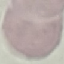
Result: no malaria parasites detected. Acquired by smartphone through the microscope eyepiece. Cell patch, automatically extracted from a larger field of view and resized to 64 × 64 pixels. Thin blood smear. Giemsa-stained preparation.